Report the malaria status of this cell.
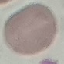

Uninfected.

Giemsa stain. Thin blood film. Automatically extracted cell patch, resized to 64 × 64 pixels. Photographed with a smartphone camera at the microscope eyepiece.